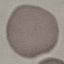
Result: no malaria parasites seen. Giemsa-stained preparation. Thin smear of blood. Cell patch, automatically extracted from a larger field of view and resized to 64 × 64 pixels. Photographed with a smartphone camera at the microscope eyepiece.